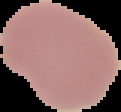
Summary:
  - Result: negative for malaria parasites
  - Preparation: thin blood smear
  - Image type: segmented cell region with the area outside set to black
  - Image size: 121×112 pixels